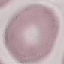
Result: no malaria parasites seen. Giemsa-stained preparation. Thin blood smear. Automatically extracted cell patch, resized to 64 × 64 pixels. Acquired by smartphone through the microscope eyepiece.